Describe the morphology of the erythrocytes.
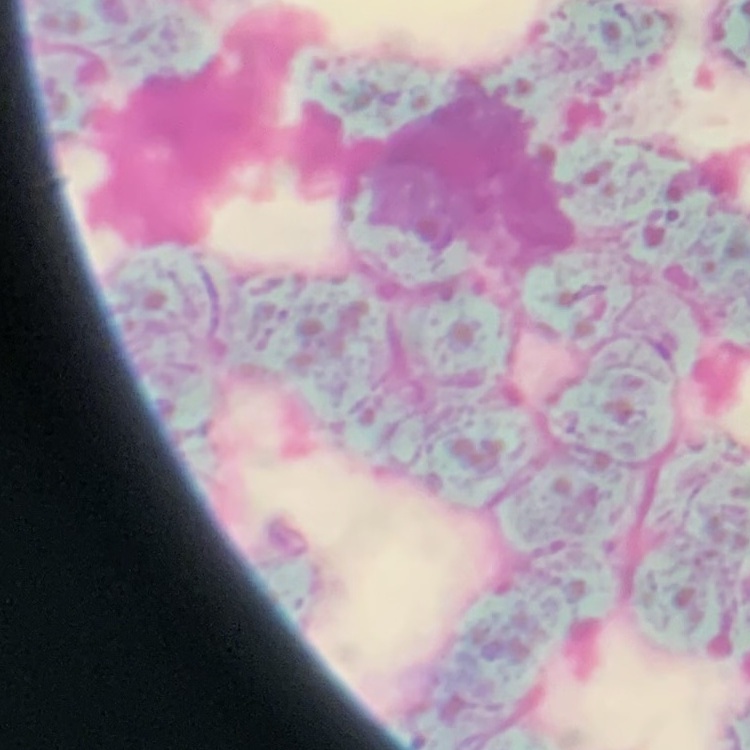

They show rouleaux formation.

Summary:
  - Preparation: thin blood smear
  - Image type: square crop of a larger photomicrograph
  - Stain: Field's or Giemsa